Identify the parasite.
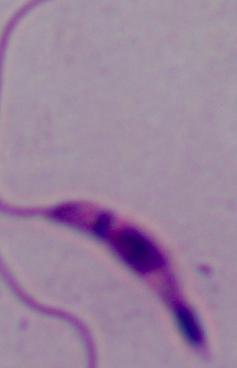

Leishmania.

magnification: 1000x
modality: photomicrograph